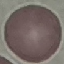

result = no malaria parasites seen
preparation = thin blood smear
image type = automatically extracted cell patch, resized to 64 × 64 pixels
capture = smartphone camera at the microscope eyepiece
stain = Giemsa